Identify the preparation type.
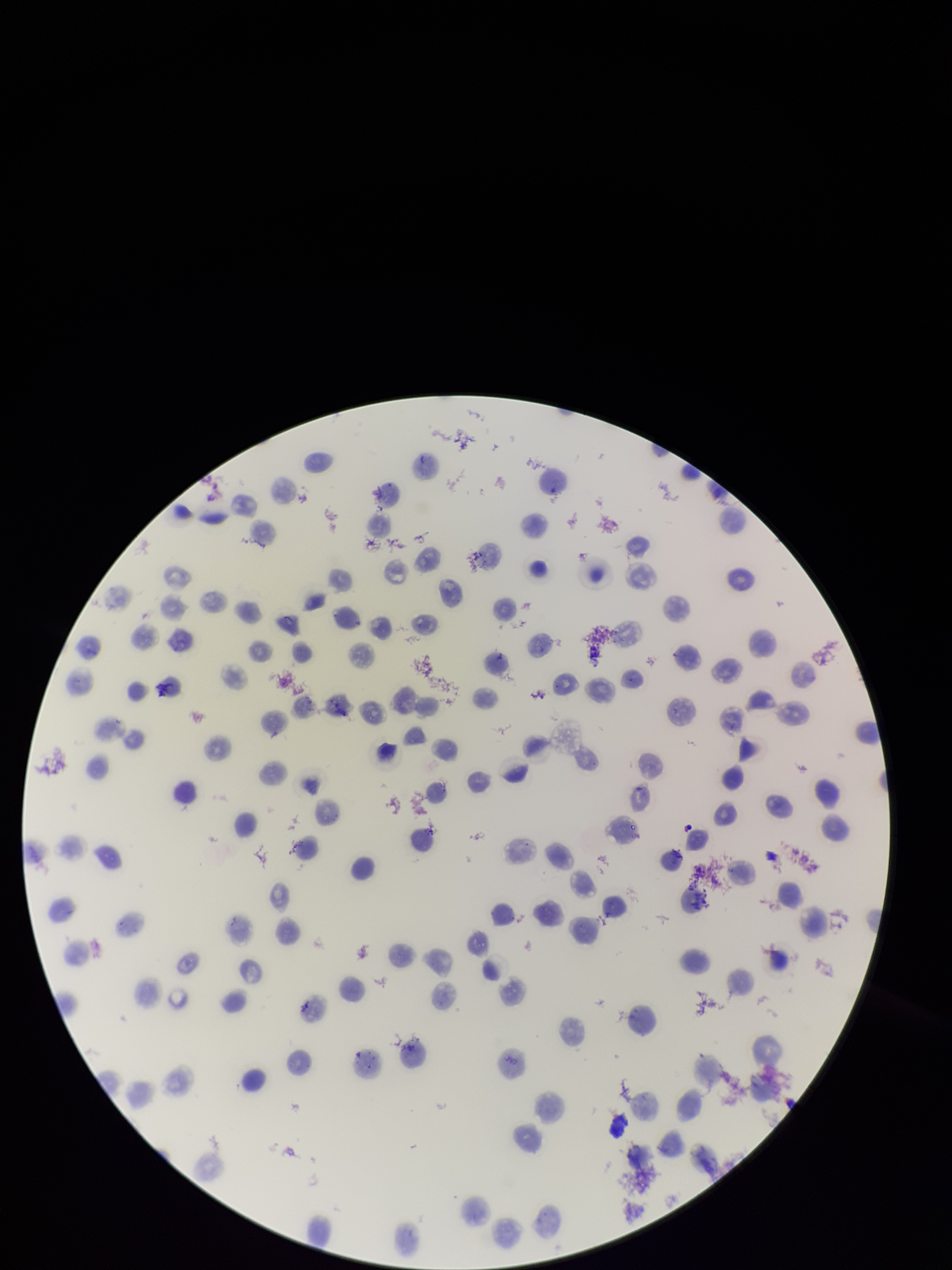

A thin smear.

One field from this slide. Patient malaria status: infected. Giemsa stain. Smartphone photograph taken through the eyepiece of a microscope. Image is 952×1270 pixels. Parasitized red blood cell count: 0. Species reported for this patient: Plasmodium vivax. Red blood cell count: 132. Parasitized red blood cells: none seen.